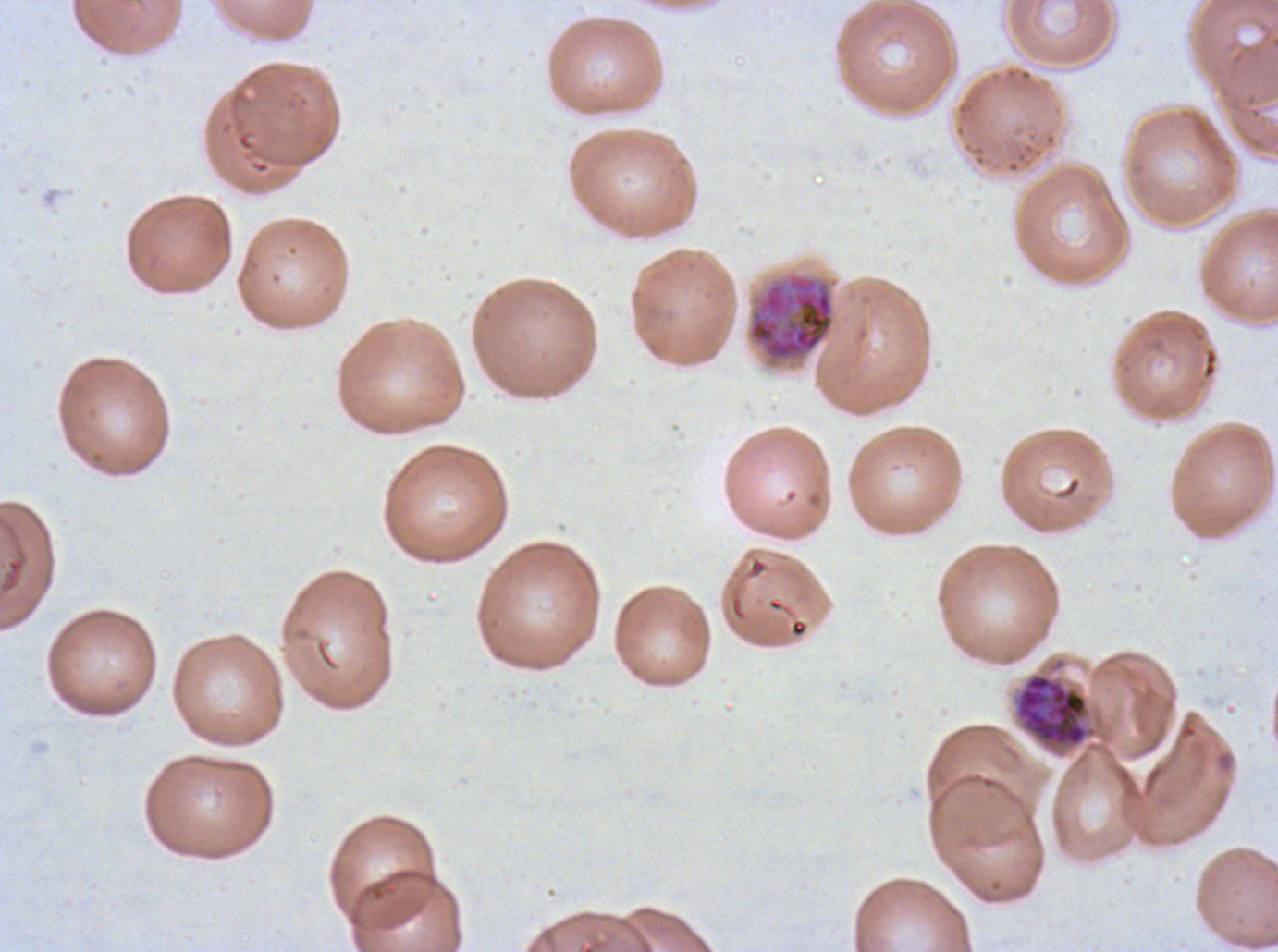

Approximate bounding boxes as [x1, y1, x2, y2] in pixels.
Summary:
  - Early schizont locations: [747, 274, 835, 361], [1014, 673, 1096, 749]
  - Specimen: P. falciparum from a patient in The Gambia, cultured ex vivo for 24 to 48 hours
  - Image size: 1278×952 pixels
  - Preparation: thin blood smear
  - Field of view: sub-image separated from a larger composite
  - Stain: Giemsa